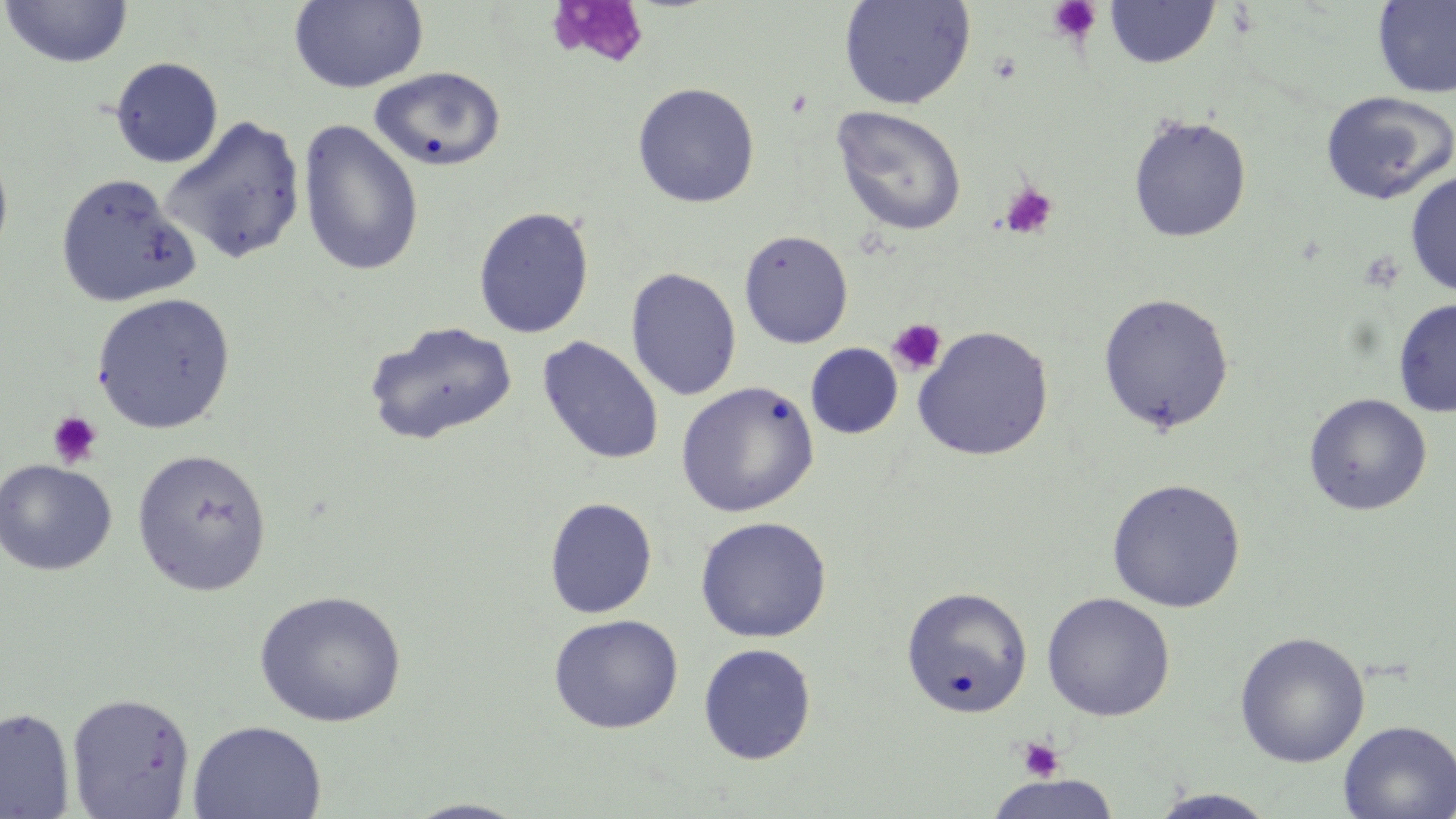

slide-level diagnosis = negative for blood parasites
platelet locations (subset) = approximate bounding boxes as (x1,y1)-(x2,y2) corner pairs in pixels: (1046,0)-(1103,44), (988,52)-(1023,84), (998,182)-(1058,240), (886,318)-(948,376), (46,411)-(104,468), (1016,736)-(1065,781)
magnification = 1000x
stain = May-Grünwald-Giemsa
image size = 1456×819 pixels
preparation = thin blood film
modality = optical microscopy
field of view = single
uninfected red blood cell locations (subset) = approximate bounding boxes as (x1,y1)-(x2,y2) corner pairs in pixels: (290,0)-(429,93), (838,0)-(976,110), (1,1)-(133,69), (1104,1)-(1220,69), (1372,1)-(1456,98), (109,56)-(224,168), (369,67)-(507,172), (632,82)-(760,208), (1320,90)-(1455,205), (831,105)-(967,236), (1126,113)-(1253,243), (160,115)-(307,265), (297,118)-(425,277), (0,147)-(14,265), (1405,171)-(1456,296), (54,172)-(200,308), (472,206)-(595,339), (738,229)-(853,349), (625,268)-(742,400), (91,292)-(236,434), (1096,292)-(1235,434), (1393,298)-(1456,417), (363,320)-(518,446), (911,325)-(1054,461), (537,336)-(664,466), (805,343)-(903,438), (675,381)-(819,518), (1303,392)-(1432,516), (131,449)-(273,596), (0,459)-(117,576), (1106,478)-(1246,613), (544,497)-(658,619), (694,515)-(832,643), (901,586)-(1034,717), (254,590)-(407,727), (1041,592)-(1176,721), (548,613)-(684,734), (1234,631)-(1370,768), (697,643)-(817,764), (66,693)-(196,818), (0,707)-(76,818), (1338,719)-(1456,819), (187,720)-(326,819), (983,775)-(1122,819), (1147,788)-(1280,818), (402,798)-(532,818)